Name the blood parasite species.
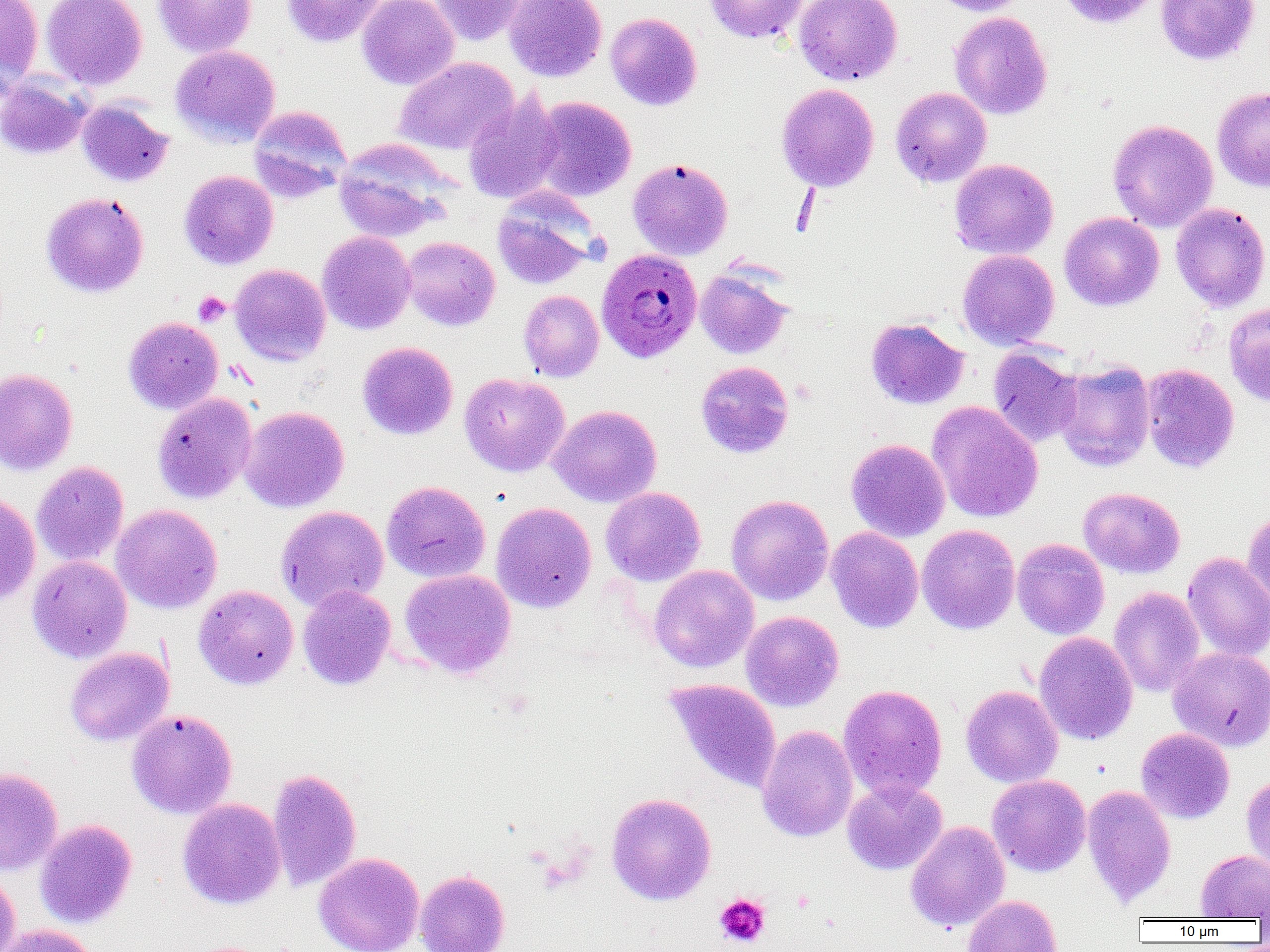

Plasmodium ovale.

Summary:
  - Coordinate format: approximate bounding boxes as named x1/y1/x2/y2 corners in pixels
  - Uninfected red blood cell locations: (x1=0, y1=0, x2=44, y2=94), (x1=41, y1=0, x2=147, y2=90), (x1=153, y1=0, x2=256, y2=57), (x1=281, y1=0, x2=387, y2=47), (x1=357, y1=0, x2=459, y2=90), (x1=428, y1=0, x2=524, y2=45), (x1=504, y1=0, x2=607, y2=82), (x1=703, y1=0, x2=809, y2=44), (x1=794, y1=0, x2=902, y2=85), (x1=928, y1=0, x2=1034, y2=16), (x1=1056, y1=0, x2=1162, y2=28), (x1=1155, y1=0, x2=1260, y2=65), (x1=949, y1=11, x2=1053, y2=120), (x1=605, y1=12, x2=703, y2=111), (x1=170, y1=44, x2=281, y2=147), (x1=177, y1=49, x2=277, y2=269), (x1=394, y1=57, x2=518, y2=155), (x1=0, y1=76, x2=91, y2=160), (x1=776, y1=83, x2=879, y2=191), (x1=1212, y1=86, x2=1270, y2=192), (x1=890, y1=87, x2=992, y2=187), (x1=463, y1=93, x2=564, y2=204), (x1=532, y1=96, x2=636, y2=202), (x1=77, y1=100, x2=174, y2=188), (x1=249, y1=106, x2=351, y2=201), (x1=1107, y1=119, x2=1218, y2=232), (x1=334, y1=139, x2=452, y2=241), (x1=627, y1=157, x2=733, y2=260), (x1=949, y1=159, x2=1058, y2=259), (x1=179, y1=170, x2=278, y2=270), (x1=491, y1=190, x2=600, y2=290), (x1=40, y1=191, x2=150, y2=298), (x1=1170, y1=203, x2=1270, y2=312), (x1=1059, y1=212, x2=1164, y2=311), (x1=317, y1=230, x2=415, y2=334), (x1=402, y1=236, x2=500, y2=330), (x1=957, y1=249, x2=1059, y2=350), (x1=230, y1=264, x2=331, y2=366), (x1=695, y1=267, x2=793, y2=359), (x1=518, y1=290, x2=604, y2=381), (x1=1224, y1=301, x2=1270, y2=407), (x1=123, y1=316, x2=223, y2=414), (x1=866, y1=318, x2=969, y2=409), (x1=357, y1=341, x2=458, y2=440), (x1=988, y1=347, x2=1083, y2=447), (x1=1054, y1=360, x2=1156, y2=472), (x1=695, y1=361, x2=794, y2=458), (x1=1141, y1=363, x2=1239, y2=473), (x1=0, y1=367, x2=78, y2=476), (x1=459, y1=372, x2=570, y2=477), (x1=152, y1=392, x2=257, y2=504), (x1=927, y1=401, x2=1044, y2=523), (x1=548, y1=404, x2=662, y2=507), (x1=239, y1=406, x2=349, y2=513), (x1=846, y1=438, x2=950, y2=542), (x1=32, y1=461, x2=129, y2=567), (x1=381, y1=480, x2=490, y2=583), (x1=600, y1=486, x2=706, y2=586), (x1=1078, y1=487, x2=1185, y2=578), (x1=0, y1=493, x2=40, y2=605), (x1=726, y1=494, x2=834, y2=606), (x1=491, y1=502, x2=596, y2=613), (x1=111, y1=504, x2=223, y2=614), (x1=276, y1=505, x2=389, y2=611), (x1=1242, y1=511, x2=1270, y2=605), (x1=916, y1=524, x2=1020, y2=634), (x1=826, y1=526, x2=924, y2=633), (x1=1012, y1=538, x2=1109, y2=640), (x1=1182, y1=552, x2=1270, y2=662), (x1=28, y1=555, x2=132, y2=663), (x1=649, y1=565, x2=759, y2=673), (x1=400, y1=569, x2=516, y2=678), (x1=193, y1=585, x2=299, y2=689), (x1=297, y1=585, x2=396, y2=690), (x1=1109, y1=587, x2=1205, y2=697), (x1=741, y1=610, x2=844, y2=712), (x1=1034, y1=632, x2=1138, y2=745), (x1=65, y1=647, x2=173, y2=746), (x1=1167, y1=647, x2=1270, y2=752), (x1=664, y1=679, x2=782, y2=793), (x1=838, y1=684, x2=948, y2=802), (x1=961, y1=685, x2=1063, y2=788), (x1=127, y1=709, x2=237, y2=818), (x1=757, y1=725, x2=858, y2=842), (x1=1136, y1=728, x2=1235, y2=823), (x1=0, y1=767, x2=63, y2=875), (x1=267, y1=767, x2=362, y2=892), (x1=1241, y1=774, x2=1270, y2=877), (x1=987, y1=775, x2=1091, y2=877), (x1=842, y1=779, x2=947, y2=875), (x1=1082, y1=785, x2=1176, y2=906), (x1=606, y1=792, x2=716, y2=905), (x1=177, y1=798, x2=286, y2=909), (x1=35, y1=819, x2=137, y2=929), (x1=905, y1=821, x2=1010, y2=932), (x1=1196, y1=849, x2=1270, y2=920), (x1=313, y1=853, x2=424, y2=952), (x1=415, y1=869, x2=510, y2=952), (x1=0, y1=870, x2=21, y2=952), (x1=963, y1=895, x2=1063, y2=952), (x1=0, y1=924, x2=100, y2=952)
  - Plasmodium ovale-infected red blood cell locations: (x1=595, y1=248, x2=703, y2=363)
  - Platelet locations: (x1=193, y1=291, x2=230, y2=327), (x1=714, y1=893, x2=770, y2=948)
  - Modality: optical microscopy
  - Preparation: thin blood smear
  - Image size: 1270×952 pixels
  - Field of view: one of a larger specimen
  - Magnification: 1000x